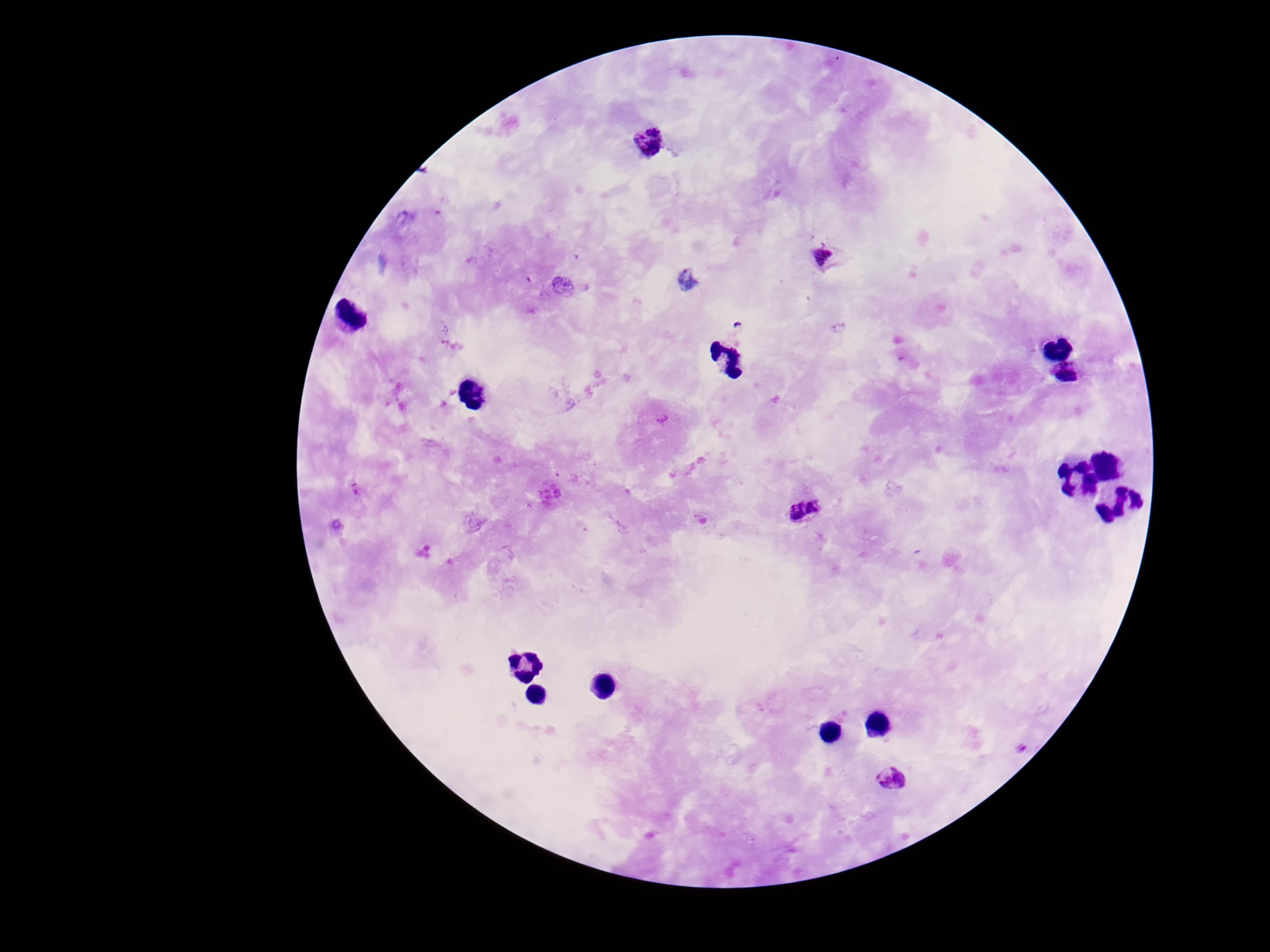
Approximate centers as (x, y) in pixels.
Summary:
  - Plasmodium parasite locations: (649, 143), (821, 256), (805, 509), (894, 779)
  - Field of view: one from this slide
  - Capture: smartphone camera through the microscope eyepiece
  - Magnification: 100x
  - Preparation: thick blood smear
  - Patient malaria status: infected
  - Image size: 1270×952 pixels
  - Stain: Giemsa